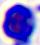
{
  "modality": "micrograph",
  "identification": "white blood cell",
  "magnification": "400x"
}